Identify the parasite.
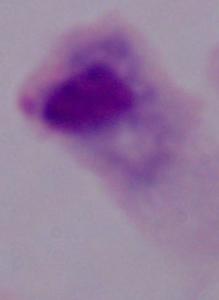

A trichomonad.

Photomicrograph. 1000x magnification.